Outline each Plasmodium malariae-infected red blood cell.
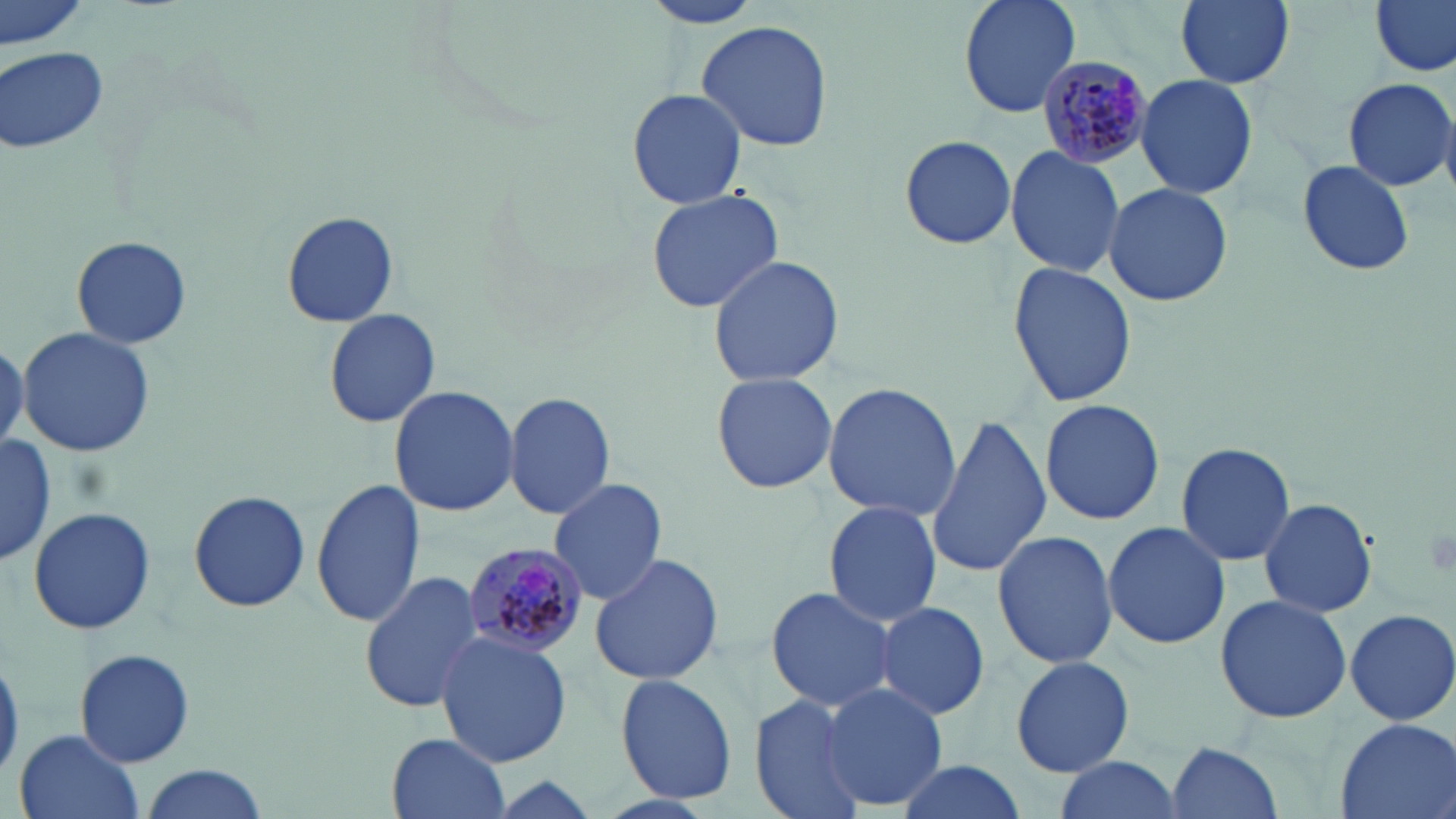
Approximate bounding boxes as [x1, y1, x2, y2] in pixels.
Plasmodium malariae-infected red blood cells: [1036, 54, 1154, 169], [460, 542, 583, 658].

Uninfected red blood cell locations: [2, 0, 89, 52], [955, 0, 1082, 120], [1172, 0, 1298, 90], [1372, 0, 1454, 76], [639, 2, 771, 27], [697, 22, 834, 151], [1, 45, 111, 156], [1135, 71, 1257, 200], [1341, 75, 1454, 193], [624, 88, 747, 210], [899, 136, 1016, 248], [1004, 144, 1126, 279], [1295, 158, 1416, 279], [1102, 181, 1234, 307], [645, 187, 784, 313], [281, 212, 399, 327], [71, 236, 191, 349], [707, 253, 845, 389], [1007, 262, 1136, 407], [323, 307, 441, 428], [17, 327, 155, 458], [0, 341, 28, 451], [710, 372, 838, 496], [821, 381, 961, 521], [389, 386, 521, 516], [504, 390, 616, 519], [1041, 399, 1165, 525], [926, 412, 1051, 579], [0, 433, 53, 568], [1175, 441, 1296, 568], [312, 478, 428, 628], [549, 478, 667, 607], [188, 490, 310, 612], [1256, 496, 1378, 618], [823, 500, 945, 627], [29, 506, 156, 634], [1102, 522, 1230, 650], [992, 529, 1119, 670], [588, 553, 725, 687], [357, 570, 484, 715], [766, 585, 898, 714], [1213, 594, 1354, 723], [873, 602, 992, 722], [1346, 609, 1456, 726], [434, 630, 574, 769], [76, 647, 196, 768], [0, 651, 24, 784], [1010, 655, 1135, 777], [615, 673, 737, 803], [818, 681, 947, 811], [753, 695, 871, 819], [1333, 717, 1455, 819], [12, 727, 147, 819], [385, 732, 510, 819], [1166, 741, 1286, 819], [1053, 755, 1180, 819], [894, 758, 1025, 819], [134, 765, 272, 819]. Slide-level diagnosis: Plasmodium malariae. Thin blood smear. Light microscopy. Captured at 1000x magnification. May-Grünwald-Giemsa-stained preparation. One field of a larger specimen. Image is 1456×819 pixels.